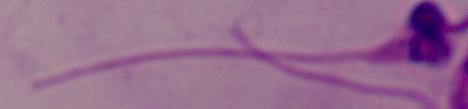

modality: photomicrograph
identification: Leishmania
magnification: 1000x